Comment on the morphology of the erythrocytes.
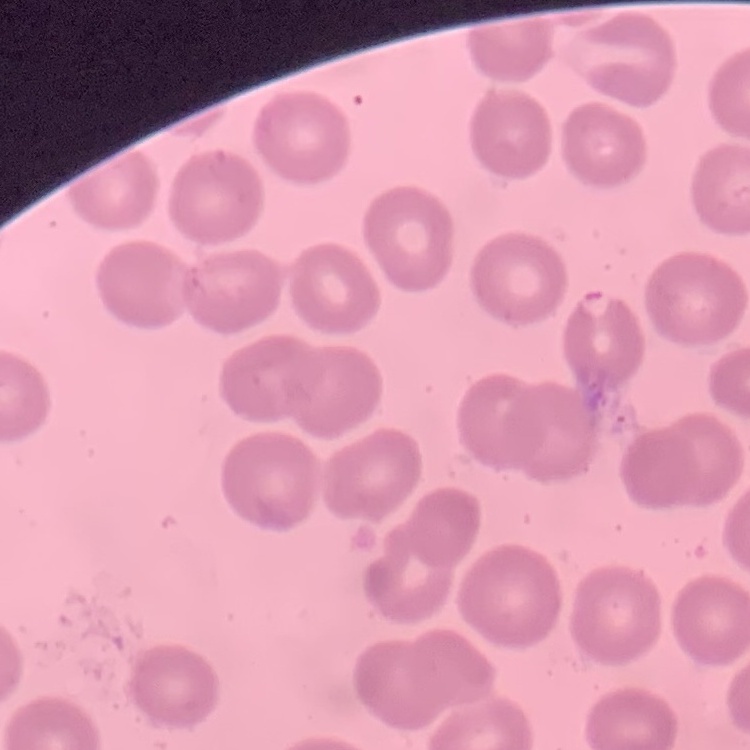
They show no rouleaux formation.

Thin peripheral smear. One tile cut from a larger photomicrograph. Stained with either Field's or Giemsa.